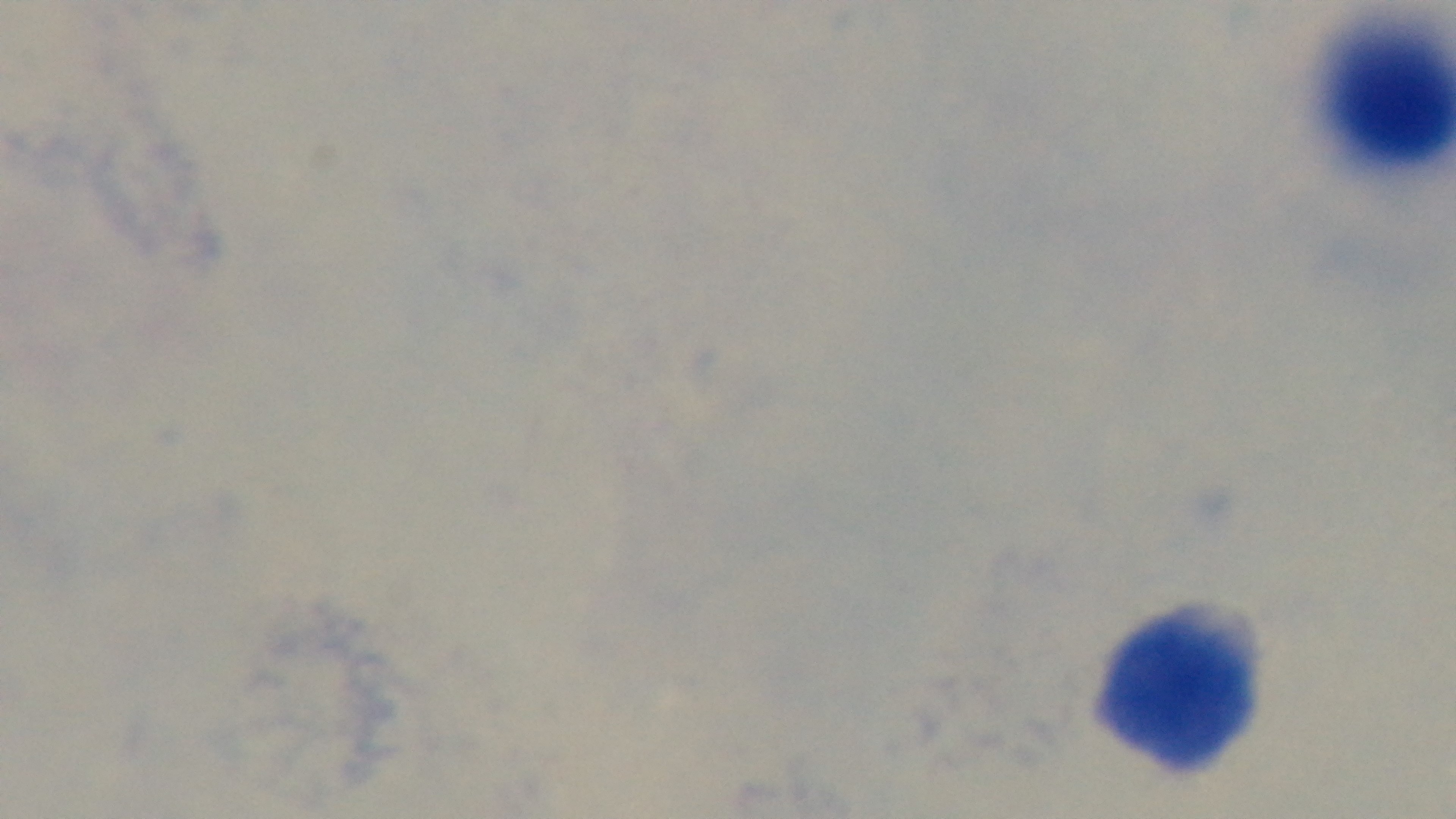
Malaria status: negative. Mounted 4K digital camera. 100x oil-immersion objective. Giemsa stain. Preparation: thick blood film. Photomicrograph. Single field of view.